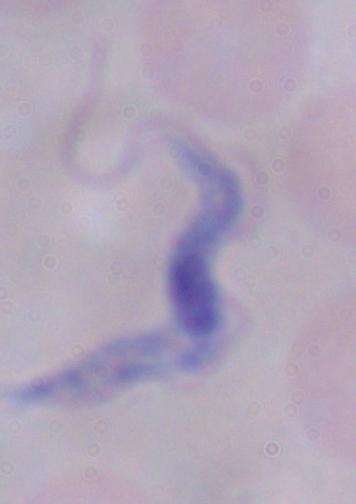

identification = trypanosome
modality = photomicrograph
magnification = 1000x